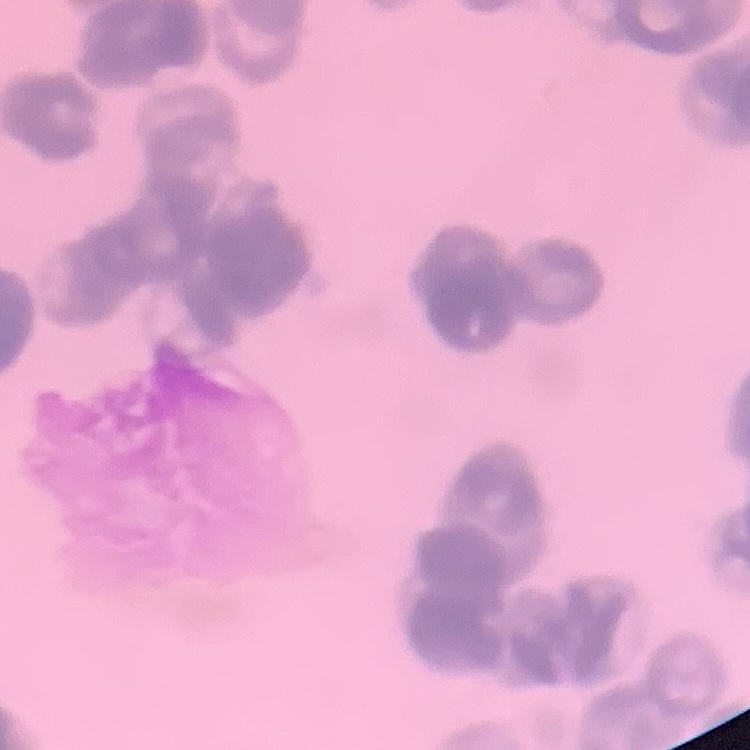
Summary:
  - Red blood cell morphology: rouleaux formation
  - Image type: one tile cut from a larger photomicrograph
  - Stain: Field's or Giemsa
  - Preparation: thin blood smear